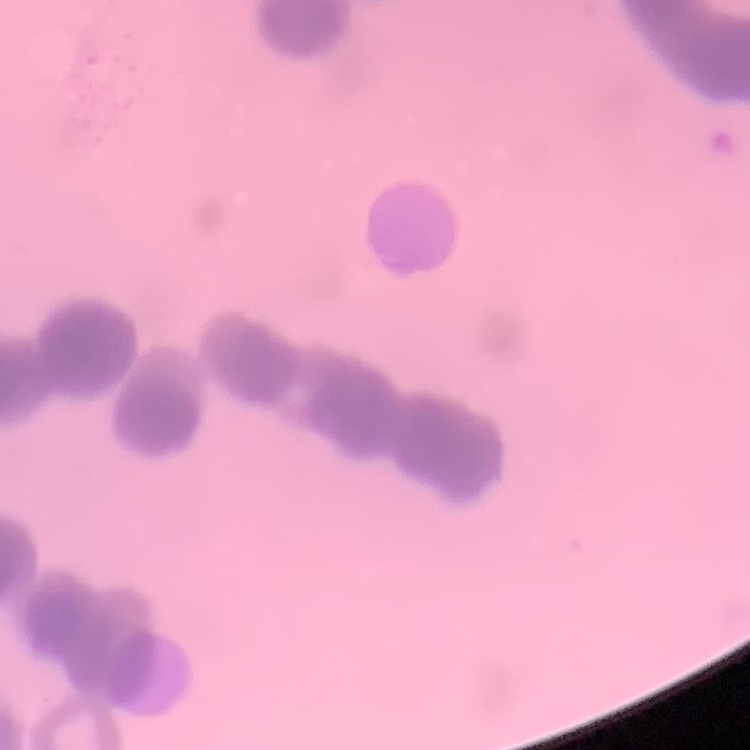
erythrocyte morphology = rouleaux formation
stain = Field's or Giemsa
image type = one tile cut from a larger photomicrograph
preparation = thin blood film